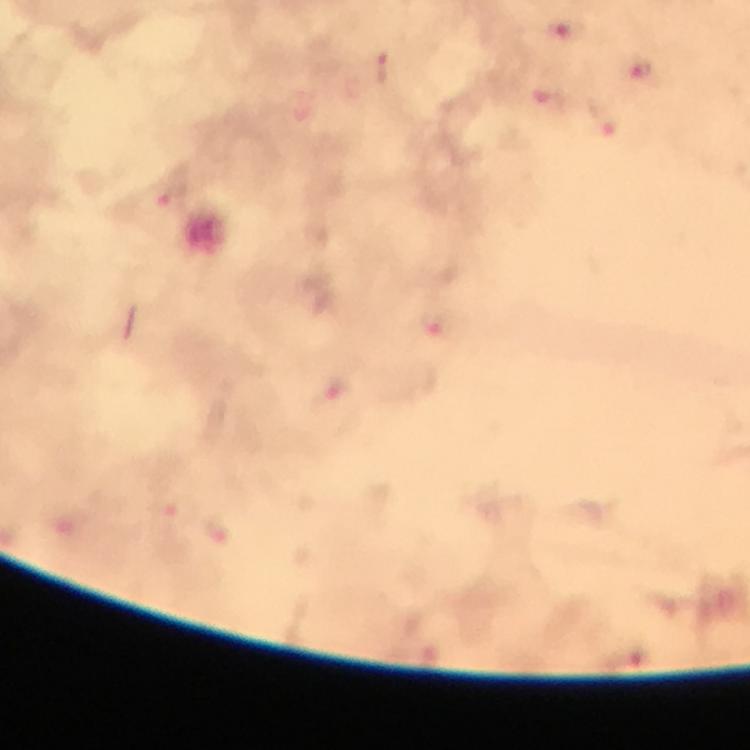
Approximate centers as [x, y] in pixels. Plasmodium parasite locations: [567, 29], [383, 66], [644, 71], [551, 97], [604, 120], [173, 197], [432, 322], [331, 388]. Image is 750×750 pixels. A crop from one field of view. Immersion oil was used. Giemsa-stained preparation. Smartphone photograph taken through a microscope. At 100x magnification. From a diagnostic examination for malaria. Thick blood smear.